Locate every leukocyte (white blood cell).
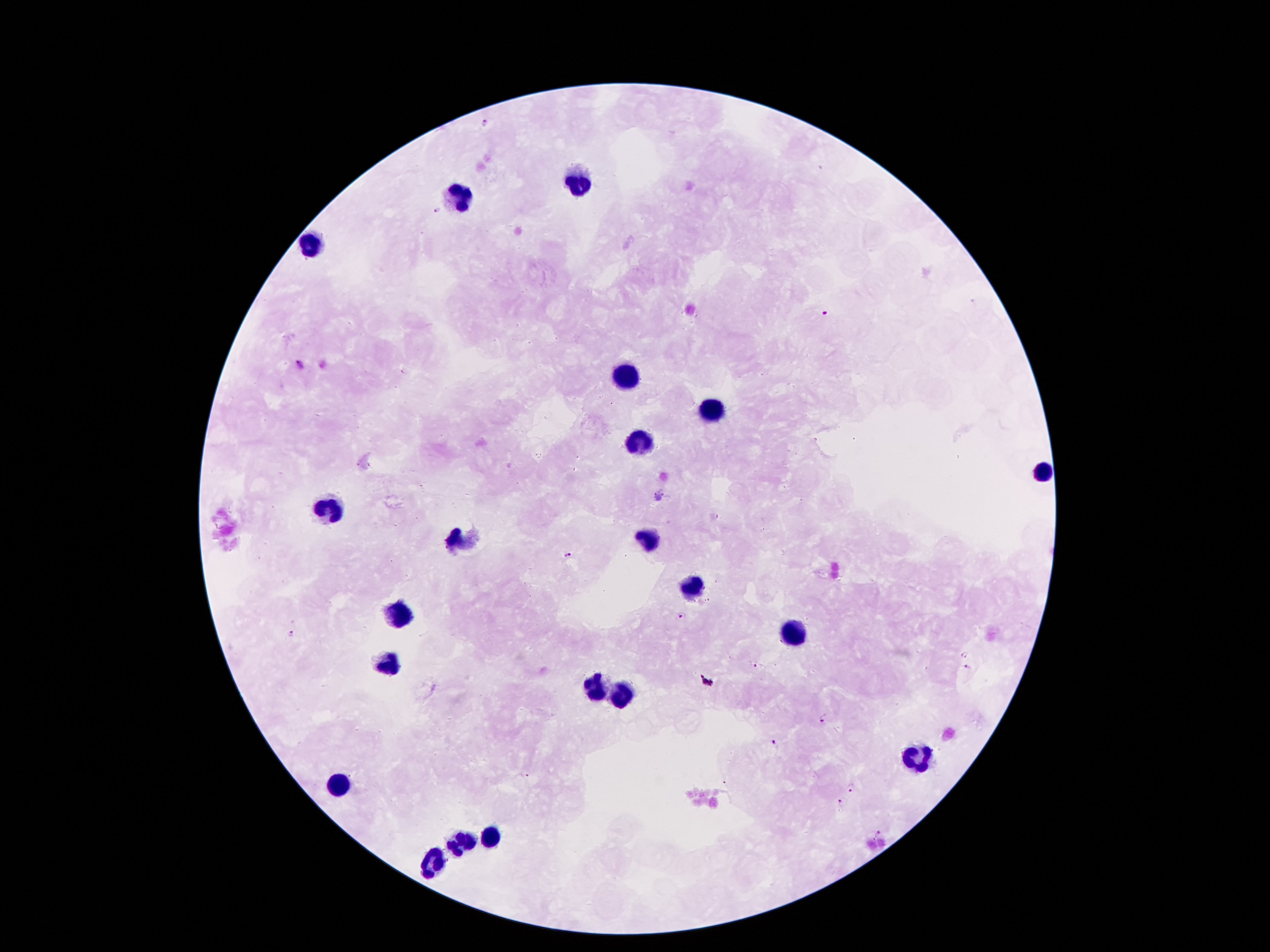
Approximate centers as (x, y) in pixels.
Leukocytes: (585, 184), (463, 202), (316, 248), (629, 372), (708, 410), (639, 446), (1044, 471), (333, 509), (461, 542), (648, 542), (696, 585), (393, 614), (797, 631), (389, 665), (591, 688), (618, 695), (914, 758), (339, 782), (492, 837), (463, 841), (435, 862).

Summary:
  - Plasmodium parasite locations: (484, 121), (437, 212), (824, 315), (299, 365), (567, 555), (684, 617), (290, 634), (966, 655), (754, 664), (968, 668), (824, 719), (773, 743), (850, 788), (843, 803), (880, 833)
  - Field of view: single
  - Image size: 1270×952 pixels
  - Preparation: thick peripheral-blood smear
  - Stain: Giemsa
  - Patient malaria status: infected with Plasmodium falciparum
  - Capture: smartphone through the microscope eyepiece
  - Magnification: 100x